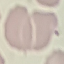

{
  "malaria_status": "uninfected",
  "capture": "smartphone through the microscope eyepiece",
  "stain": "Giemsa",
  "preparation": "thin blood film",
  "image_type": "cell patch, automatically extracted from a larger field of view and resized to 64 × 64 pixels"
}